Assess this cell for malaria.
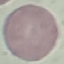
Uninfected.

Summary:
  - Stain: Giemsa
  - Capture: smartphone through the microscope eyepiece
  - Image type: automatically extracted cell patch, resized to 64 × 64 pixels
  - Preparation: thin blood film